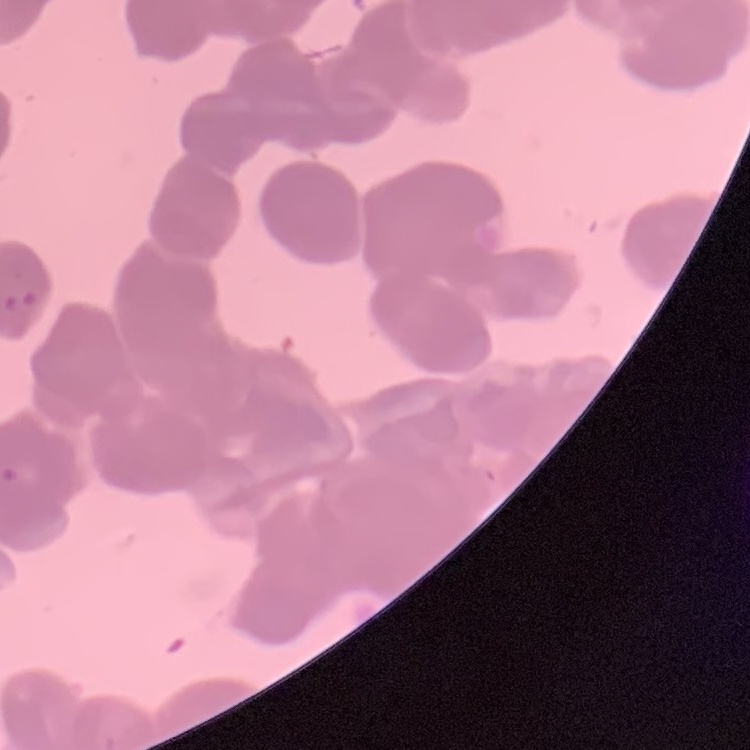
Summary:
  - Red blood cell morphology: rouleaux formation
  - Preparation: thin peripheral smear
  - Image type: one tile cut from a larger photomicrograph
  - Stain: Field's or Giemsa